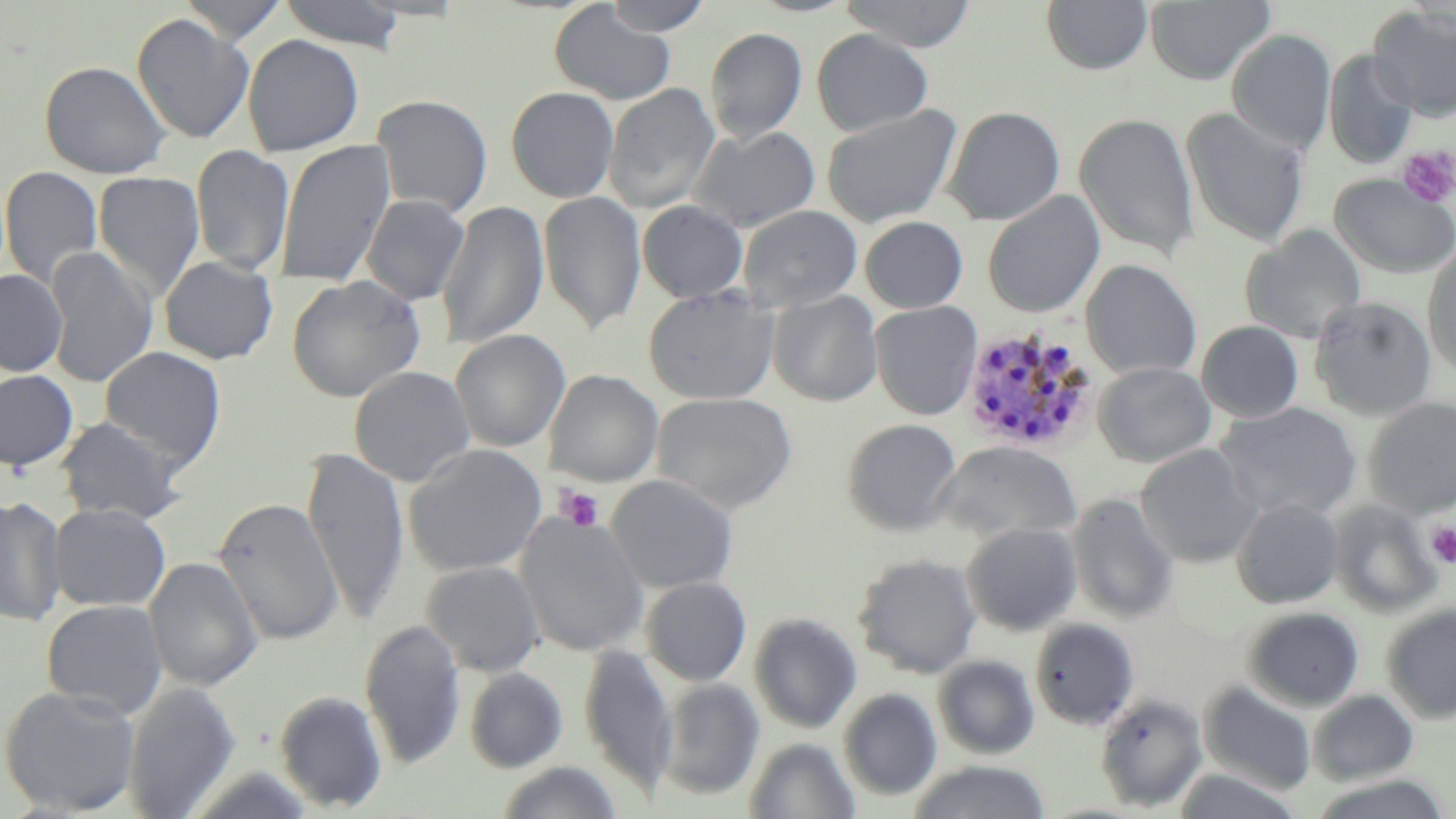
slide-level diagnosis = Plasmodium malariae
platelet locations = approximate bounding boxes as named x1/y1/x2/y2 corners in pixels: (x1=1396, y1=145, x2=1456, y2=208), (x1=555, y1=485, x2=606, y2=533), (x1=1425, y1=522, x2=1456, y2=567)
magnification = 1000x
field of view = single
image size = 1456×819 pixels
stain = May-Grünwald-Giemsa
Plasmodium malariae-infected red blood cell locations = approximate bounding boxes as named x1/y1/x2/y2 corners in pixels: (x1=960, y1=324, x2=1099, y2=455)
modality = light microscopy
preparation = thin blood smear
uninfected red blood cell locations = approximate bounding boxes as named x1/y1/x2/y2 corners in pixels: (x1=177, y1=0, x2=290, y2=43), (x1=601, y1=0, x2=715, y2=36), (x1=838, y1=0, x2=978, y2=52), (x1=1041, y1=0, x2=1154, y2=76), (x1=277, y1=1, x2=409, y2=52), (x1=1145, y1=1, x2=1276, y2=85), (x1=549, y1=3, x2=677, y2=105), (x1=1368, y1=5, x2=1456, y2=120), (x1=132, y1=13, x2=254, y2=144), (x1=705, y1=27, x2=808, y2=145), (x1=1226, y1=28, x2=1336, y2=155), (x1=810, y1=29, x2=933, y2=137), (x1=242, y1=34, x2=364, y2=157), (x1=1324, y1=49, x2=1418, y2=170), (x1=39, y1=61, x2=172, y2=179), (x1=604, y1=82, x2=720, y2=215), (x1=506, y1=86, x2=619, y2=203), (x1=372, y1=95, x2=493, y2=218), (x1=821, y1=104, x2=962, y2=228), (x1=942, y1=106, x2=1066, y2=226), (x1=1180, y1=107, x2=1310, y2=247), (x1=1074, y1=112, x2=1200, y2=262), (x1=690, y1=125, x2=820, y2=232), (x1=275, y1=139, x2=395, y2=284), (x1=191, y1=144, x2=295, y2=276), (x1=1, y1=167, x2=103, y2=290), (x1=93, y1=171, x2=206, y2=301), (x1=1329, y1=174, x2=1456, y2=279), (x1=538, y1=191, x2=647, y2=335), (x1=982, y1=191, x2=1105, y2=318), (x1=361, y1=195, x2=469, y2=305), (x1=436, y1=199, x2=549, y2=351), (x1=638, y1=200, x2=748, y2=303), (x1=738, y1=204, x2=862, y2=312), (x1=860, y1=216, x2=968, y2=313), (x1=1240, y1=225, x2=1368, y2=343), (x1=1422, y1=244, x2=1456, y2=381), (x1=45, y1=245, x2=157, y2=388), (x1=159, y1=256, x2=278, y2=365), (x1=1081, y1=260, x2=1202, y2=380), (x1=0, y1=269, x2=67, y2=376), (x1=287, y1=275, x2=426, y2=402), (x1=643, y1=286, x2=780, y2=405), (x1=768, y1=290, x2=884, y2=407), (x1=1310, y1=295, x2=1438, y2=420), (x1=870, y1=300, x2=983, y2=421), (x1=1197, y1=321, x2=1305, y2=423), (x1=451, y1=329, x2=570, y2=452), (x1=100, y1=346, x2=226, y2=470), (x1=1093, y1=361, x2=1216, y2=467), (x1=349, y1=366, x2=476, y2=487), (x1=0, y1=369, x2=78, y2=472), (x1=544, y1=369, x2=664, y2=488), (x1=652, y1=392, x2=797, y2=514), (x1=1363, y1=397, x2=1456, y2=518), (x1=1215, y1=402, x2=1362, y2=521), (x1=55, y1=416, x2=187, y2=524), (x1=842, y1=418, x2=962, y2=536), (x1=935, y1=441, x2=1082, y2=546), (x1=403, y1=443, x2=548, y2=578), (x1=1136, y1=443, x2=1261, y2=568), (x1=303, y1=446, x2=409, y2=624), (x1=606, y1=474, x2=739, y2=594), (x1=1067, y1=492, x2=1180, y2=624), (x1=0, y1=494, x2=67, y2=627), (x1=213, y1=497, x2=344, y2=645), (x1=1232, y1=498, x2=1344, y2=608), (x1=1328, y1=499, x2=1442, y2=618), (x1=48, y1=503, x2=171, y2=612), (x1=516, y1=510, x2=650, y2=657), (x1=961, y1=522, x2=1083, y2=636), (x1=853, y1=553, x2=982, y2=678), (x1=145, y1=556, x2=263, y2=692), (x1=422, y1=561, x2=545, y2=677), (x1=641, y1=577, x2=752, y2=686), (x1=41, y1=599, x2=168, y2=720), (x1=1381, y1=602, x2=1456, y2=723), (x1=1243, y1=606, x2=1365, y2=712), (x1=749, y1=612, x2=863, y2=733), (x1=1030, y1=617, x2=1140, y2=730), (x1=359, y1=619, x2=467, y2=770), (x1=579, y1=644, x2=678, y2=797), (x1=933, y1=655, x2=1040, y2=759), (x1=464, y1=667, x2=568, y2=773), (x1=658, y1=677, x2=764, y2=801), (x1=122, y1=681, x2=241, y2=818), (x1=1199, y1=681, x2=1317, y2=796), (x1=1, y1=685, x2=141, y2=816), (x1=838, y1=688, x2=942, y2=801), (x1=1308, y1=689, x2=1419, y2=786), (x1=275, y1=692, x2=388, y2=812), (x1=1095, y1=692, x2=1208, y2=811), (x1=744, y1=736, x2=861, y2=818), (x1=907, y1=760, x2=1051, y2=819), (x1=494, y1=761, x2=624, y2=819), (x1=1171, y1=767, x2=1305, y2=818), (x1=1306, y1=775, x2=1453, y2=819)